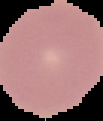

Summary:
  - Result: no malaria parasites detected
  - Image type: cell region segmented out of the field of view; surrounding area masked to black
  - Image size: 103×121 pixels
  - Preparation: thin blood smear